Classify this cell by malaria status.
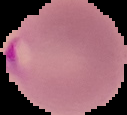
It is parasitized.

Summary:
  - Preparation: thin blood film
  - Image type: segmented cell region on a black background
  - Image size: 127×115 pixels